Outline each Plasmodium ovale-infected red blood cell.
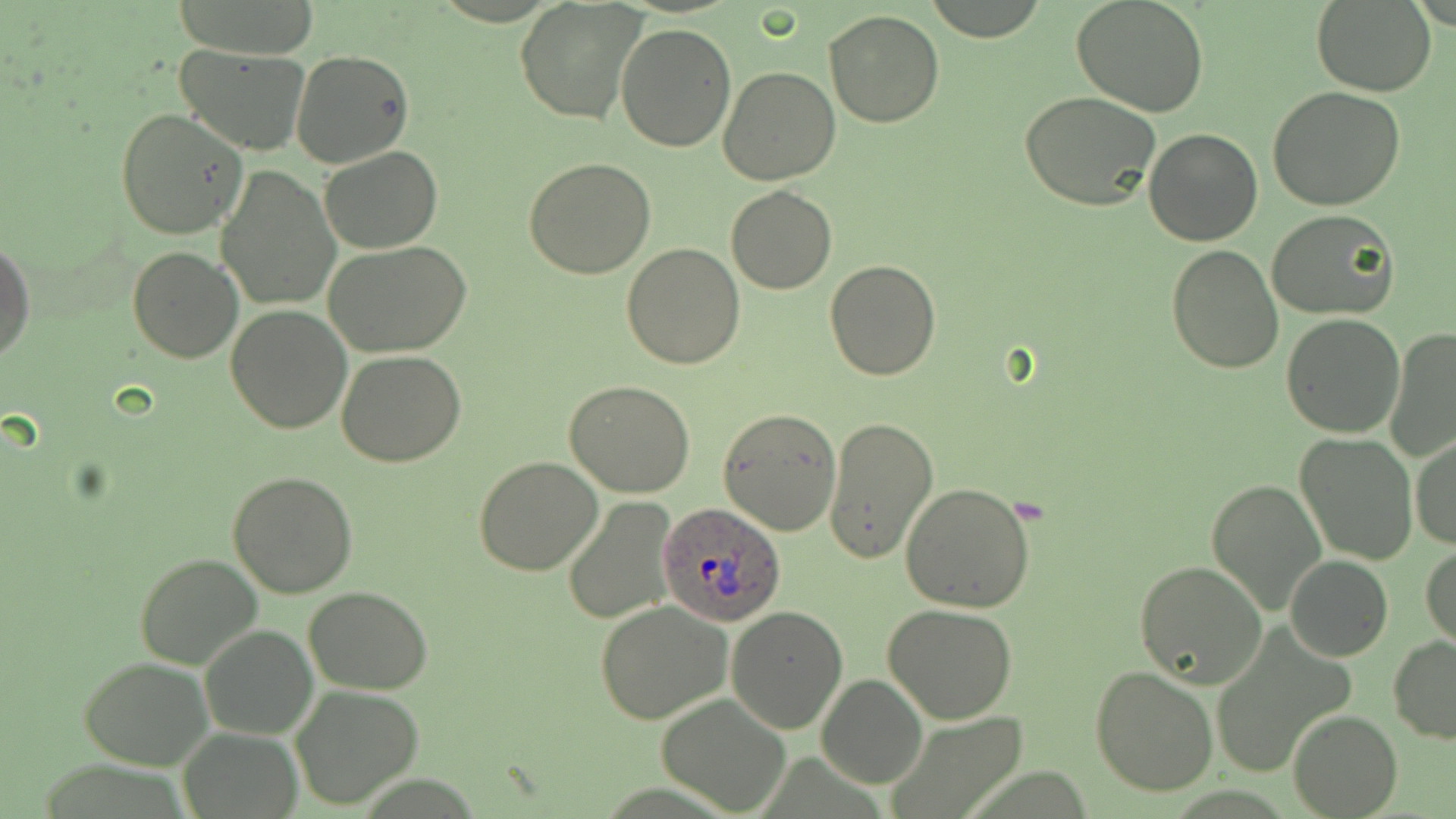
Approximate bounding boxes as (x1,y1)-(x2,y2) corner pairs in pixels.
Plasmodium ovale-infected red blood cells: (656,504)-(785,627).

Summary:
  - Uninfected red blood cell locations: (924,0)-(1053,43), (1071,0)-(1210,118), (1310,0)-(1436,96), (173,1)-(320,60), (515,1)-(646,126), (823,10)-(946,127), (616,21)-(739,152), (175,44)-(311,156), (290,49)-(414,168), (718,65)-(840,184), (1268,85)-(1407,210), (1019,91)-(1162,212), (115,107)-(249,241), (1144,128)-(1263,246), (319,144)-(442,253), (523,158)-(655,278), (216,166)-(340,312), (725,184)-(837,294), (1266,210)-(1399,320), (0,239)-(35,365), (324,240)-(471,357), (623,244)-(746,369), (1165,244)-(1285,374), (127,246)-(243,363), (825,260)-(940,381), (224,305)-(351,433), (1280,314)-(1406,439), (1385,327)-(1456,464), (335,350)-(466,468), (564,381)-(695,498), (717,407)-(841,536), (823,416)-(938,565), (1295,432)-(1418,565), (1410,435)-(1455,551), (474,455)-(603,575), (226,470)-(358,597), (1204,477)-(1327,616), (901,482)-(1036,611), (562,497)-(678,625), (1421,544)-(1455,652), (135,553)-(262,668), (1284,554)-(1393,662), (1133,560)-(1266,688), (303,586)-(434,694), (594,600)-(733,724), (883,604)-(1018,723), (725,606)-(850,734), (200,624)-(316,740), (1388,636)-(1456,743), (79,656)-(213,771), (1090,665)-(1219,797), (816,674)-(927,789), (290,685)-(424,810), (654,691)-(791,815), (883,709)-(1030,819), (1287,709)-(1401,817), (178,727)-(300,819)
  - Slide-level diagnosis: Plasmodium ovale
  - Magnification: 1000x
  - Field of view: single
  - Image size: 1456×819 pixels
  - Preparation: thin blood smear
  - Modality: optical microscopy
  - Stain: May-Grünwald-Giemsa